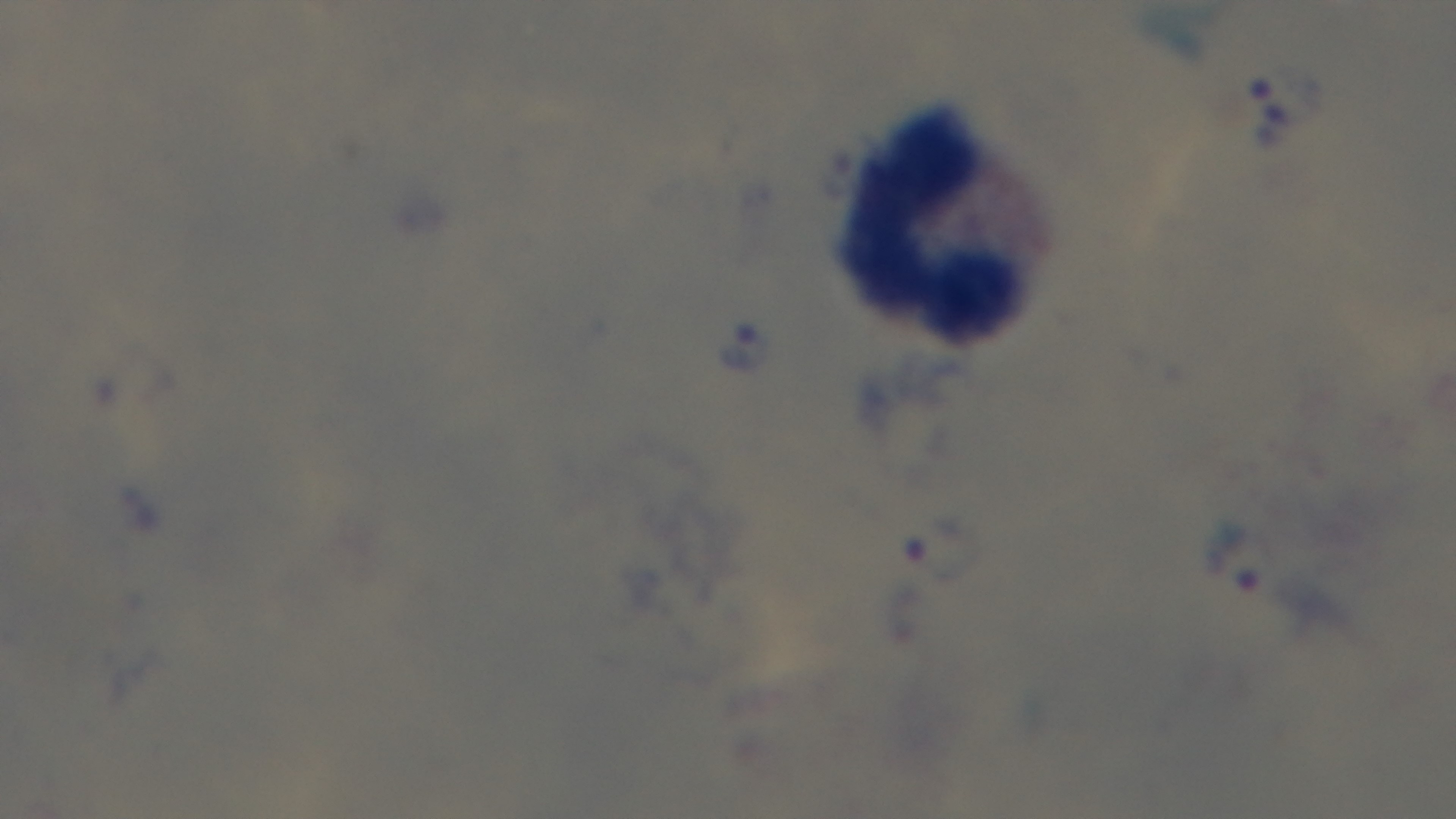

Summary:
  - Stain: Giemsa
  - Field of view: one from the slide
  - Malaria status: positive
  - Capture: mounted 4K digital camera
  - Modality: light microscopy
  - Objective: 100x oil immersion
  - Preparation: thick